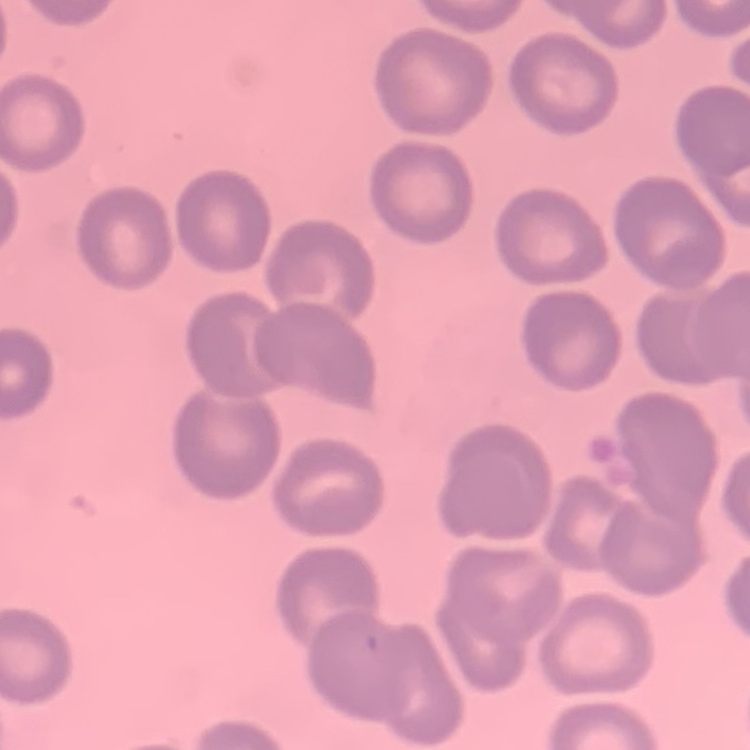 The red blood cells exhibit no rouleaux formation. Stained with either Field's or Giemsa. One tile cut from a larger photomicrograph. Thin peripheral smear.